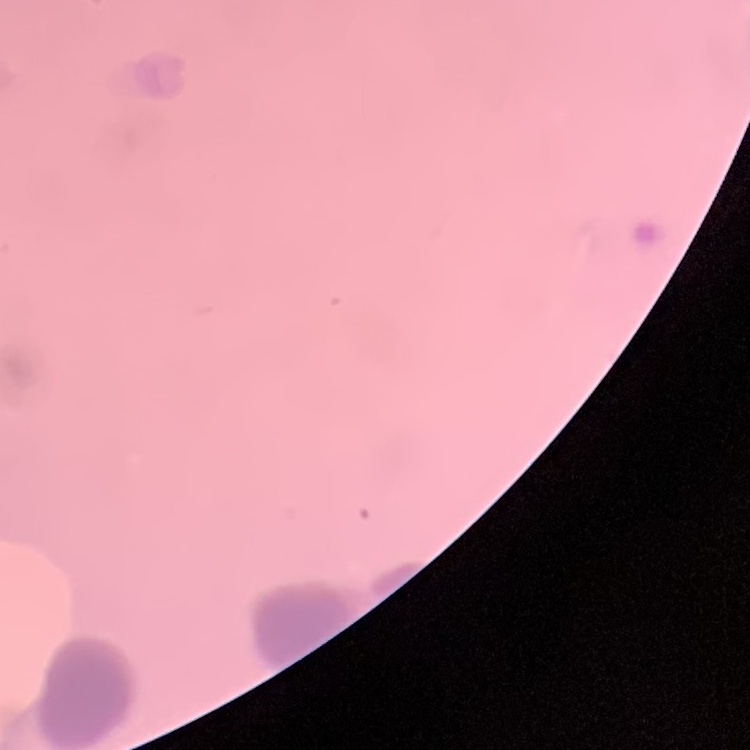
The erythrocytes show rouleaux formation. One tile cut from a larger photomicrograph. Thin blood film. Field's or Giemsa stain.